Outline each blood parasite and name the species.
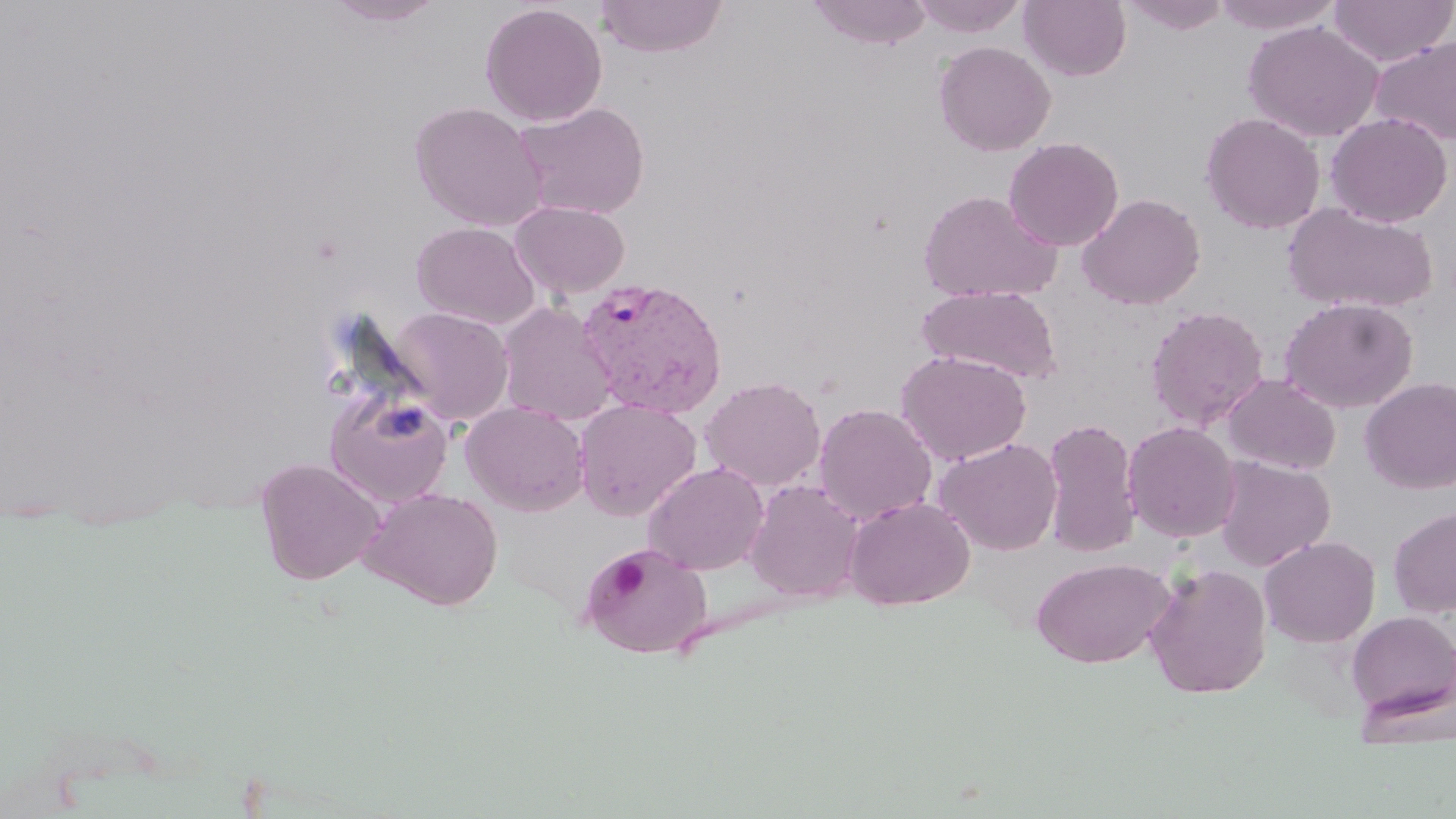
Approximate bounding boxes as (x1,y1)-(x2,y2) corner pairs in pixels.
Plasmodium vivax-infected red blood cells: (576,277)-(728,419).
No Plasmodium falciparum, Plasmodium ovale, Plasmodium malariae, Babesia divergens, or Trypanosoma brucei observed.

Uninfected red blood cell locations: (325,0)-(445,26), (595,0)-(728,58), (807,0)-(933,50), (911,0)-(1028,37), (1020,0)-(1131,81), (1120,0)-(1232,35), (1209,0)-(1345,34), (1328,0)-(1455,67), (480,3)-(608,126), (1243,20)-(1383,142), (1370,35)-(1456,145), (933,41)-(1056,156), (410,101)-(547,231), (513,101)-(650,220), (1201,112)-(1325,234), (1325,112)-(1453,228), (1003,137)-(1124,251), (917,190)-(1062,303), (1076,193)-(1205,310), (510,201)-(631,297), (1281,201)-(1437,315), (411,221)-(541,329), (917,284)-(1062,384), (1279,297)-(1418,413), (498,302)-(618,425), (1146,304)-(1269,430), (388,307)-(514,425), (896,350)-(1031,466), (1222,374)-(1341,475), (700,376)-(826,490), (1360,377)-(1456,494), (325,390)-(454,506), (574,399)-(702,520), (461,401)-(590,516), (814,403)-(938,524), (1041,418)-(1141,557), (1122,421)-(1241,543), (934,437)-(1063,555), (1214,456)-(1335,571), (254,457)-(385,585), (643,461)-(769,575), (744,479)-(865,602), (360,487)-(503,611), (845,496)-(975,610), (1388,506)-(1456,617), (1260,535)-(1380,647), (580,544)-(712,659), (1031,556)-(1175,668), (1144,563)-(1273,699), (1346,611)-(1456,722). Platelet locations: (609,556)-(648,599). Slide-level diagnosis: Plasmodium vivax. Captured at 1000x magnification. One field of a larger specimen. Image is 1456×819 pixels. May-Grünwald-Giemsa stain. Light microscopy. Thin blood smear.